Locate every Plasmodium ovale-infected red blood cell.
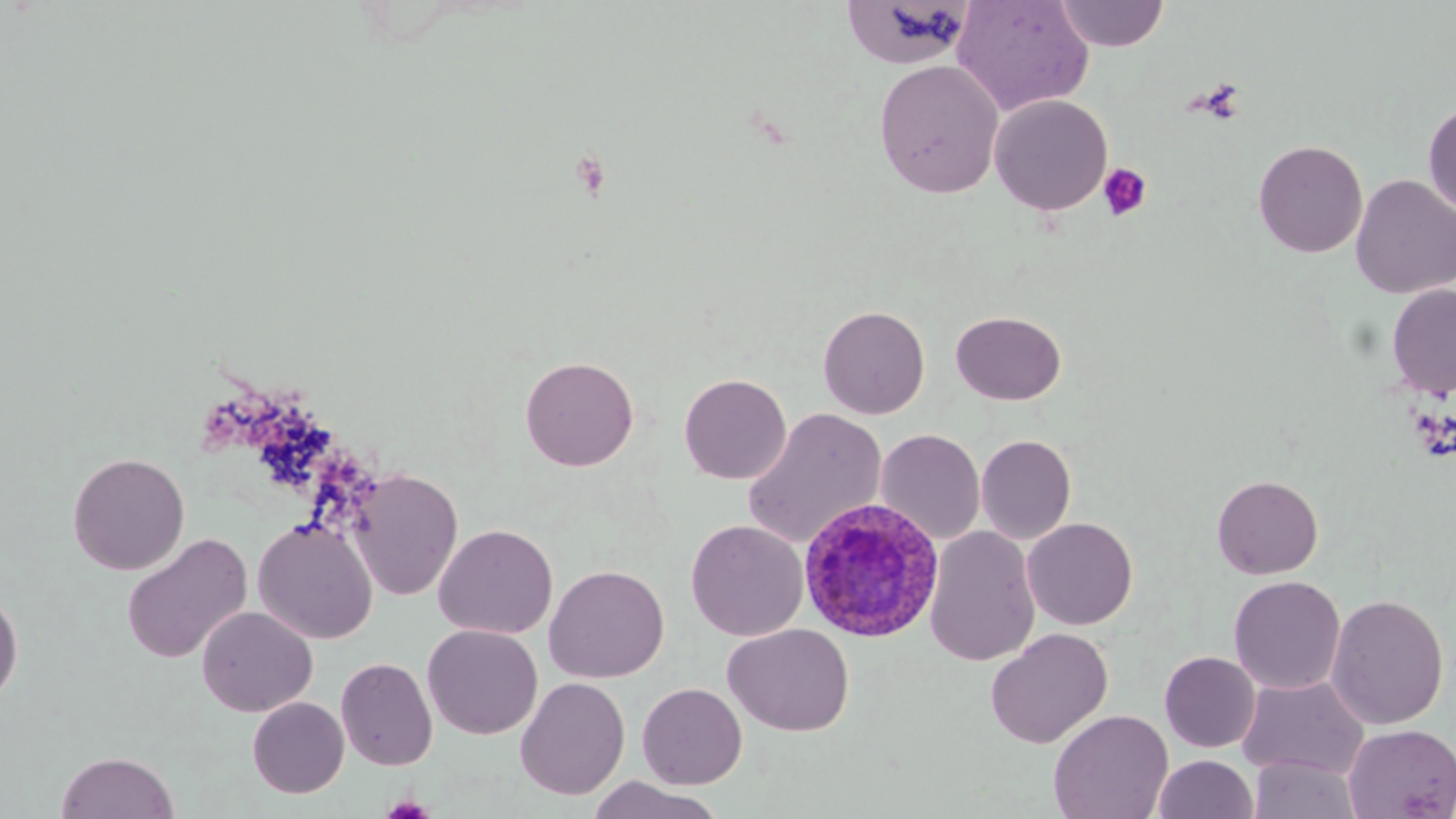

Approximate bounding boxes as (x1, y1, x2, y2) in pixels.
Plasmodium ovale-infected red blood cells: (798, 496, 944, 642).

slide-level diagnosis = Plasmodium ovale
image size = 1456×819 pixels
preparation = thin blood smear
field of view = single
magnification = 1000x
uninfected red blood cell locations = approximate bounding boxes as (x1, y1, x2, y2) in pixels: (952, 0, 1094, 116), (1054, 0, 1170, 51), (841, 1, 975, 69), (874, 60, 1004, 198), (989, 95, 1113, 215), (1422, 100, 1456, 217), (1252, 140, 1367, 258), (1350, 175, 1456, 299), (1386, 284, 1456, 399), (817, 305, 930, 419), (950, 310, 1067, 406), (520, 355, 639, 471), (679, 373, 791, 484), (741, 407, 887, 549), (875, 428, 986, 545), (976, 434, 1077, 544), (67, 451, 190, 575), (348, 468, 464, 601), (1212, 475, 1323, 579), (252, 517, 378, 644), (1022, 517, 1138, 629), (685, 519, 808, 641), (433, 523, 558, 639), (923, 526, 1041, 666), (121, 532, 253, 665), (544, 564, 670, 683), (1228, 575, 1346, 694), (0, 587, 24, 707), (1325, 593, 1449, 730), (196, 605, 318, 717), (422, 624, 543, 739), (722, 624, 855, 736), (985, 628, 1113, 749), (1159, 651, 1261, 753), (336, 657, 438, 771), (1236, 674, 1370, 780), (515, 676, 630, 800), (637, 682, 747, 789), (247, 697, 349, 798), (1048, 709, 1173, 819), (1343, 724, 1456, 818), (55, 751, 180, 818), (1153, 754, 1258, 818), (1248, 754, 1363, 818), (588, 776, 722, 819)
platelet locations = approximate bounding boxes as (x1, y1, x2, y2) in pixels: (1098, 162, 1152, 221), (379, 795, 438, 818)
modality = light microscopy
stain = May-Grünwald-Giemsa